Assess this cell for malaria.
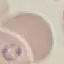

Parasitized.

Cell patch, automatically extracted from a larger field of view and resized to 64 × 64 pixels. Giemsa stain. Thin smear of blood. Photographed with a smartphone camera at the microscope eyepiece.